Report the malaria status of this cell.
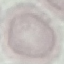
It is uninfected.

{
  "image_type": "cell patch, automatically extracted from a larger field of view and resized to 64 × 64 pixels",
  "stain": "Giemsa",
  "preparation": "thin blood smear",
  "capture": "smartphone camera at the microscope eyepiece"
}